Identify the cell.
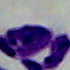

A leukocyte.

magnification = 1000x
modality = photomicrograph